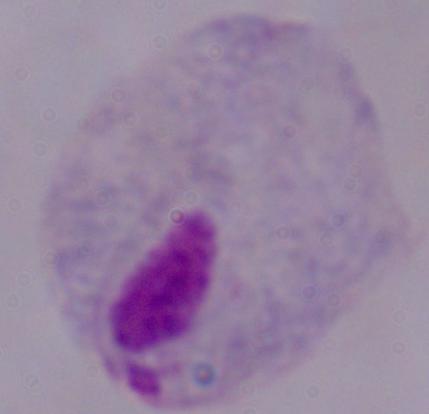

Summary:
  - Magnification: 1000x
  - Modality: micrograph
  - Identification: trichomonad